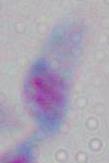

1000x magnification. Toxoplasma gondii is shown. Micrograph.